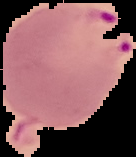

Summary:
  - Image size: 136×157 pixels
  - Preparation: thin blood film
  - Image type: cell region segmented out of the field of view; surrounding area masked to black
  - Malaria status: parasitized